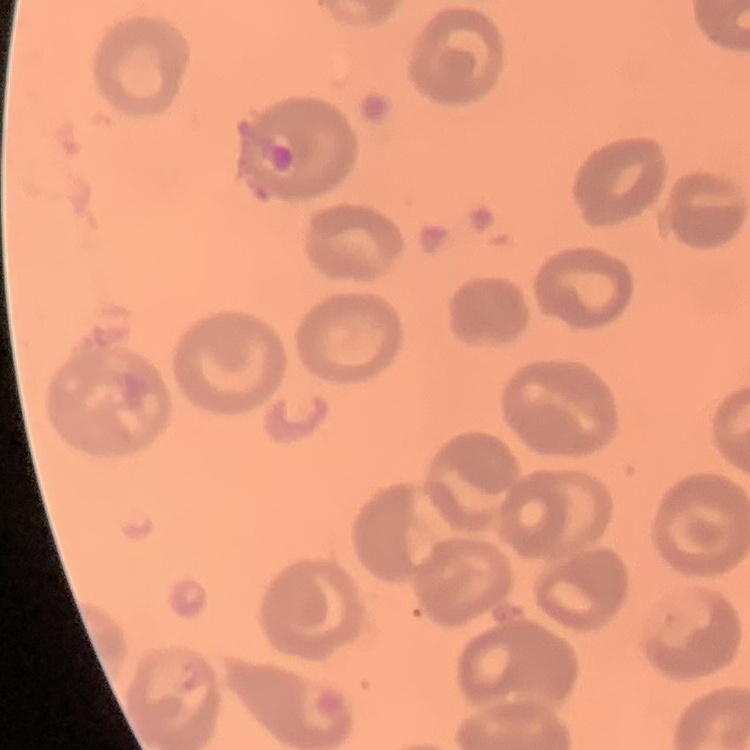

{
  "red_blood_cell_morphology": "no rouleaux formation",
  "stain": "Field's or Giemsa",
  "preparation": "thin peripheral smear",
  "image_type": "square crop of a larger photomicrograph"
}